Locate every blood parasite and identify its species.
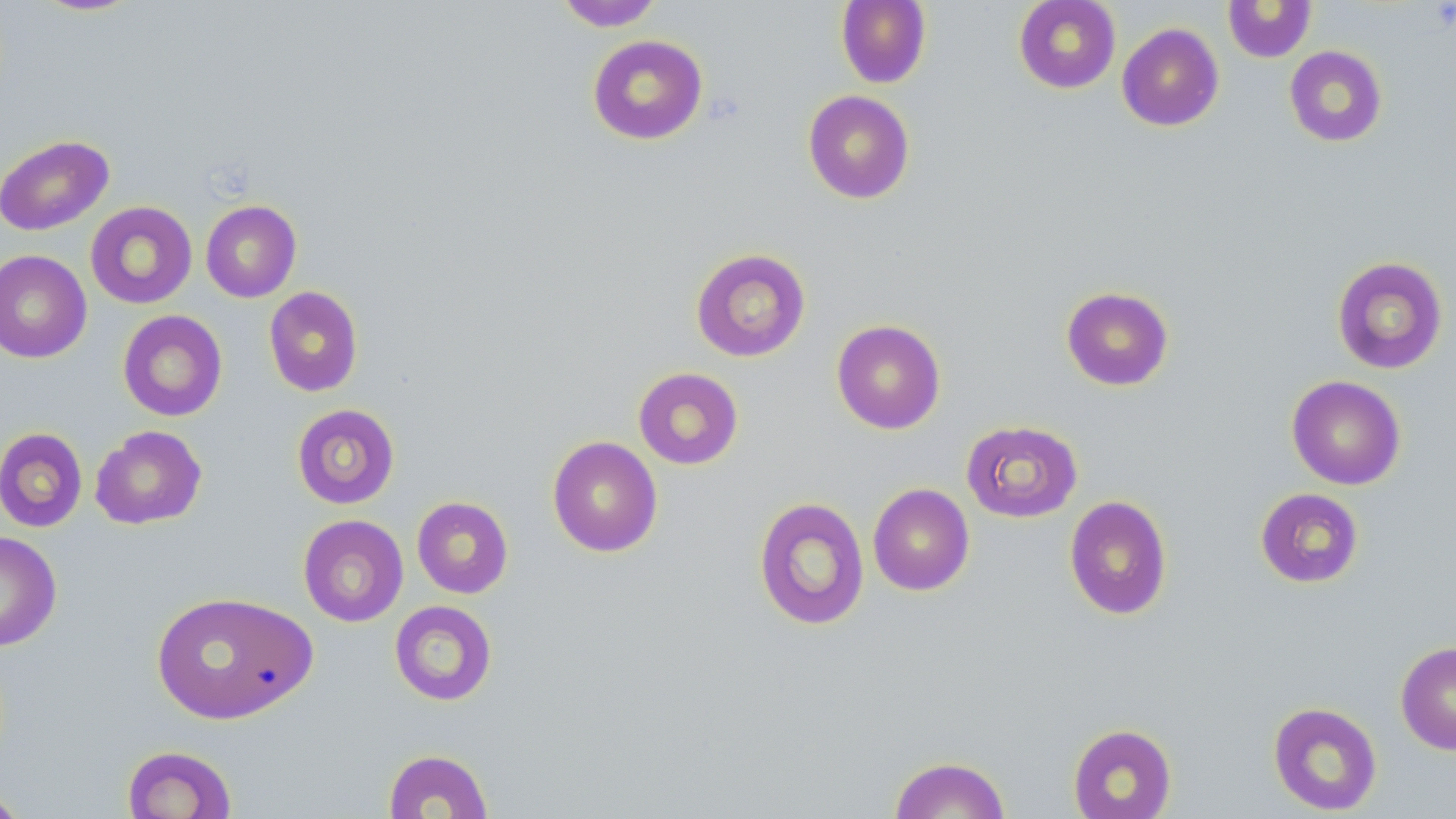

No blood parasites seen.

Approximate bounding boxes as named x1/y1/x2/y2 corners in pixels. Uninfected red blood cell locations: (x1=31, y1=0, x2=143, y2=17), (x1=836, y1=0, x2=932, y2=88), (x1=1013, y1=0, x2=1121, y2=94), (x1=555, y1=1, x2=665, y2=31), (x1=1223, y1=1, x2=1316, y2=62), (x1=1116, y1=22, x2=1224, y2=131), (x1=587, y1=34, x2=708, y2=145), (x1=1284, y1=45, x2=1388, y2=147), (x1=803, y1=90, x2=915, y2=204), (x1=0, y1=134, x2=114, y2=236), (x1=200, y1=200, x2=301, y2=302), (x1=85, y1=202, x2=198, y2=308), (x1=690, y1=248, x2=811, y2=362), (x1=0, y1=250, x2=91, y2=363), (x1=1331, y1=255, x2=1448, y2=375), (x1=263, y1=286, x2=364, y2=397), (x1=1061, y1=286, x2=1174, y2=391), (x1=117, y1=310, x2=228, y2=421), (x1=831, y1=319, x2=946, y2=434), (x1=633, y1=367, x2=744, y2=470), (x1=1286, y1=375, x2=1406, y2=490), (x1=291, y1=403, x2=400, y2=509), (x1=961, y1=420, x2=1083, y2=522), (x1=90, y1=425, x2=207, y2=529), (x1=0, y1=427, x2=88, y2=532), (x1=547, y1=436, x2=663, y2=557), (x1=868, y1=483, x2=975, y2=596), (x1=1255, y1=487, x2=1365, y2=588), (x1=1064, y1=495, x2=1173, y2=620), (x1=412, y1=496, x2=514, y2=598), (x1=752, y1=496, x2=870, y2=631), (x1=297, y1=514, x2=409, y2=627), (x1=0, y1=530, x2=62, y2=652), (x1=149, y1=590, x2=316, y2=725), (x1=389, y1=600, x2=497, y2=706), (x1=1395, y1=641, x2=1456, y2=755), (x1=1267, y1=701, x2=1383, y2=815), (x1=1067, y1=723, x2=1177, y2=819), (x1=121, y1=745, x2=237, y2=819), (x1=383, y1=748, x2=494, y2=818), (x1=888, y1=755, x2=1011, y2=818), (x1=0, y1=787, x2=30, y2=819). Slide-level diagnosis: negative for blood parasites. May-Grünwald-Giemsa-stained preparation. Single field of view. Light microscopy. Thin blood smear. 1000x magnification. Image is 1456×819 pixels.